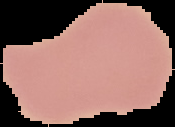
image_size: 175×127 pixels
preparation: thin blood smear
result: no malaria parasites detected
image_type: segmented cell region with the area outside set to black